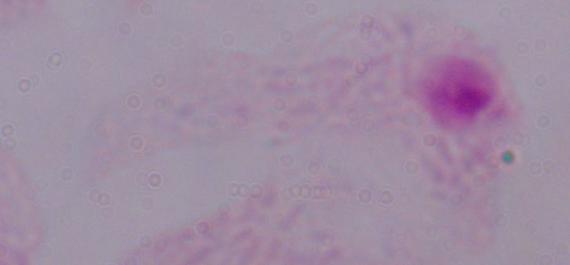
Summary:
  - Magnification: 1000x
  - Identification: trichomonad
  - Modality: micrograph